Outline each blood parasite and name the species.
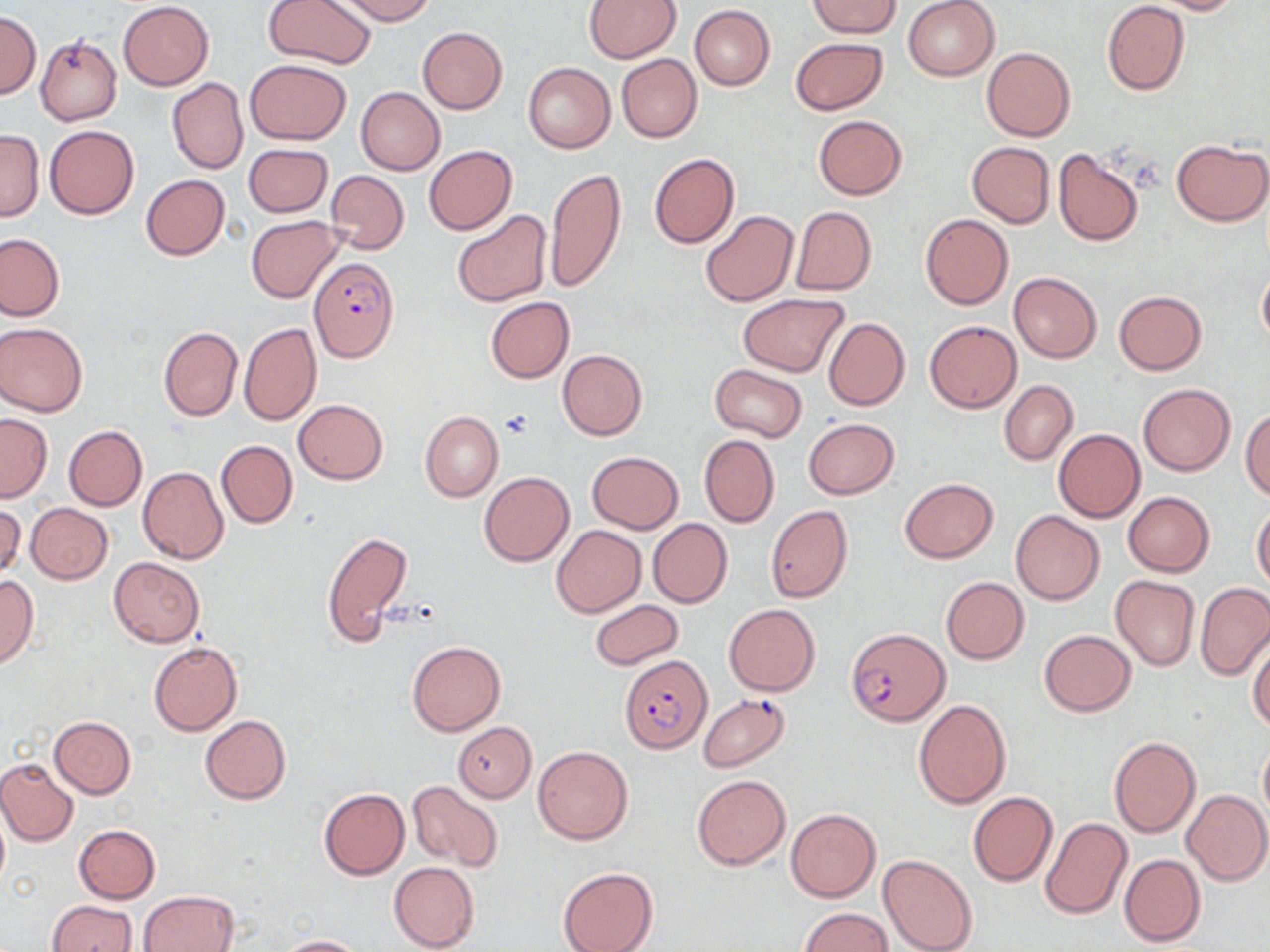
Approximate bounding boxes as [x1, y1, x2, y2] in pixels.
Plasmodium falciparum-infected red blood cells: [309, 258, 400, 363], [846, 627, 949, 725], [621, 656, 713, 753], [699, 693, 791, 771].
No Plasmodium ovale, Plasmodium malariae, Plasmodium vivax, Babesia divergens, or Trypanosoma brucei observed.

Summary:
  - Uninfected red blood cell locations: [261, 0, 378, 70], [334, 0, 436, 25], [583, 0, 680, 63], [810, 0, 900, 38], [903, 0, 999, 81], [1149, 0, 1243, 15], [117, 2, 214, 89], [1102, 2, 1189, 95], [690, 5, 775, 90], [1, 13, 40, 98], [418, 26, 508, 113], [36, 35, 122, 126], [789, 37, 887, 115], [981, 48, 1075, 141], [616, 54, 702, 144], [246, 58, 350, 144], [524, 62, 615, 152], [168, 78, 248, 173], [356, 87, 444, 175], [814, 115, 907, 199], [45, 126, 139, 219], [0, 130, 44, 221], [1170, 139, 1269, 226], [966, 142, 1055, 228], [244, 144, 333, 217], [423, 146, 517, 234], [1052, 147, 1144, 247], [649, 152, 739, 250], [544, 166, 626, 294], [326, 170, 409, 254], [140, 174, 230, 261], [789, 206, 877, 295], [453, 210, 552, 308], [700, 211, 798, 306], [919, 212, 1013, 310], [246, 216, 342, 302], [0, 233, 66, 321], [1256, 261, 1270, 347], [1008, 272, 1102, 363], [1114, 291, 1206, 374], [738, 294, 848, 377], [485, 296, 573, 382], [822, 317, 909, 411], [924, 320, 1020, 413], [0, 322, 87, 416], [239, 322, 321, 426], [159, 326, 241, 422], [558, 349, 647, 439], [709, 364, 808, 441], [998, 380, 1078, 465], [1137, 383, 1235, 476], [293, 399, 387, 483], [1241, 409, 1270, 499], [422, 411, 503, 501], [0, 414, 52, 501], [803, 418, 900, 498], [64, 425, 147, 510], [1053, 428, 1145, 522], [699, 434, 780, 527], [216, 439, 297, 528], [588, 451, 683, 532], [138, 466, 228, 563], [479, 472, 574, 567], [899, 478, 998, 563], [1122, 491, 1215, 577], [1, 502, 24, 581], [25, 503, 112, 584], [766, 505, 853, 603], [1251, 506, 1270, 589], [1010, 511, 1105, 605], [648, 519, 733, 607], [551, 525, 646, 617], [321, 531, 413, 647], [108, 556, 205, 646], [0, 574, 37, 669], [1110, 575, 1198, 672], [940, 576, 1029, 663], [1195, 583, 1270, 681], [590, 599, 683, 670], [724, 604, 819, 696], [1038, 629, 1136, 716], [1248, 639, 1270, 733], [148, 641, 241, 735], [407, 641, 505, 735], [913, 700, 1010, 809], [200, 715, 291, 804], [49, 716, 136, 798], [453, 722, 536, 801], [1109, 736, 1200, 837], [1257, 738, 1270, 823], [533, 745, 633, 845], [0, 757, 79, 846], [691, 775, 790, 869], [405, 781, 505, 873], [318, 788, 410, 880], [1182, 789, 1270, 886], [969, 791, 1057, 886], [785, 808, 880, 902], [0, 810, 9, 890], [1040, 816, 1132, 921], [73, 824, 160, 903], [878, 853, 978, 952], [1119, 853, 1206, 947], [389, 861, 480, 952], [557, 865, 658, 952], [139, 891, 238, 952], [46, 901, 137, 952], [800, 907, 895, 951], [275, 935, 366, 952]
  - Slide-level diagnosis: Plasmodium falciparum
  - Field of view: single
  - Stain: May-Grünwald-Giemsa
  - Modality: light microscopy
  - Preparation: thin blood film
  - Magnification: 1000x
  - Image size: 1270×952 pixels